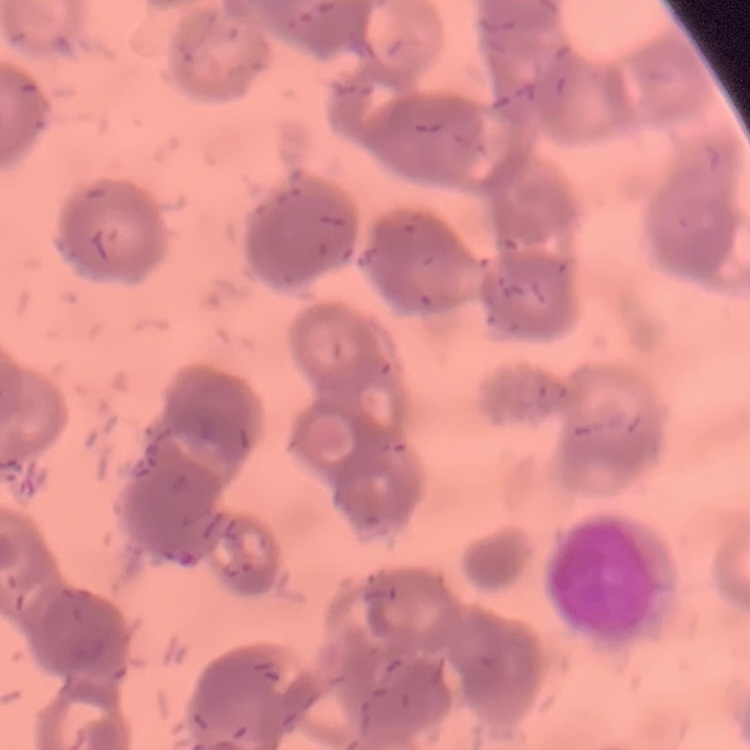

erythrocyte morphology = rouleaux formation
stain = Field's or Giemsa
preparation = thin blood film
image type = square crop of a larger photomicrograph